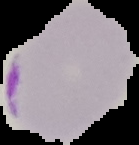
Summary:
  - Malaria status: parasitized
  - Image size: 139×145 pixels
  - Preparation: thin blood smear
  - Image type: cell region segmented out of the field of view; surrounding area masked to black